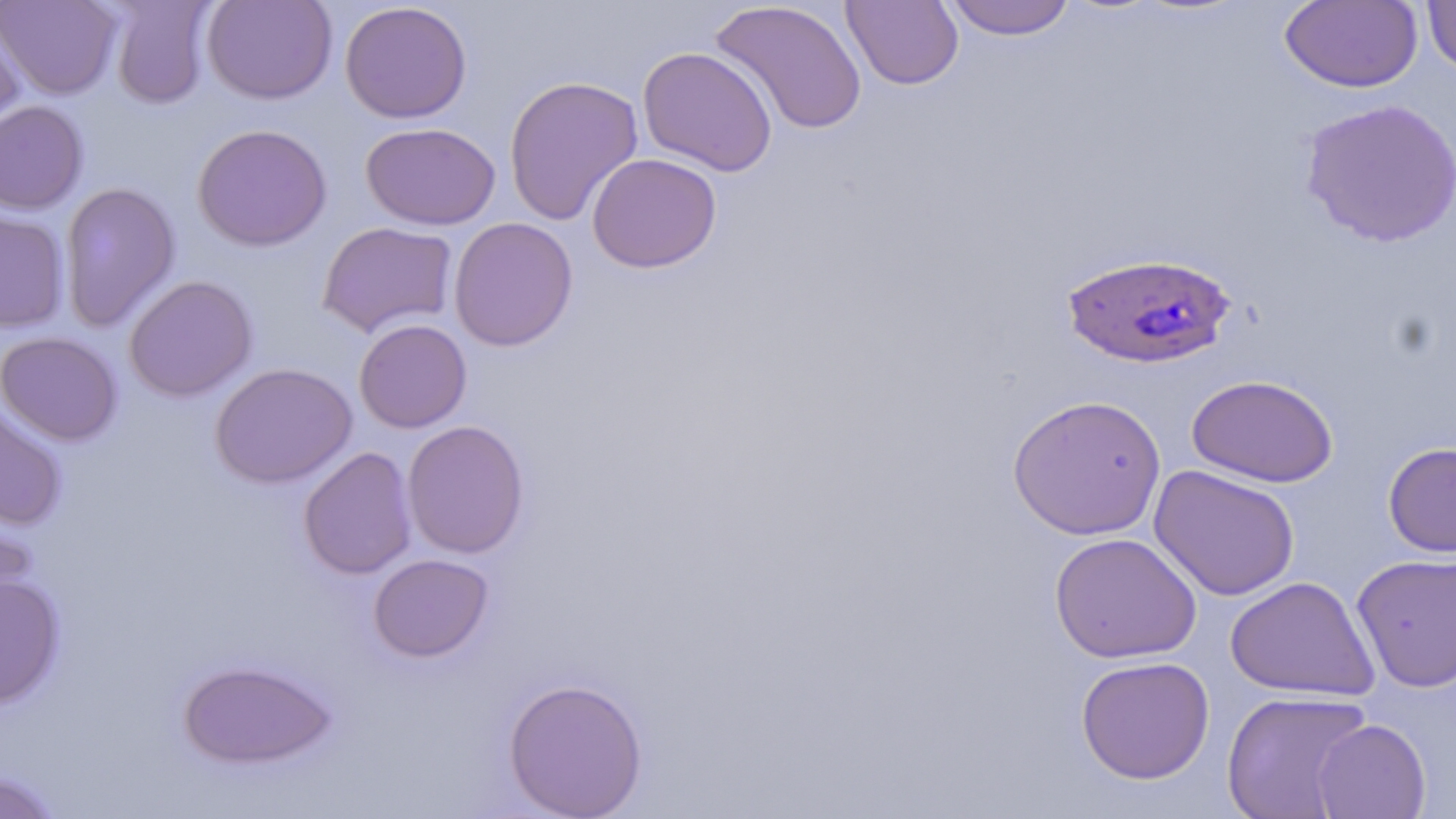
Summary:
  - Coordinate format: approximate bounding boxes as [x1, y1, x2, y2] in pixels
  - Plasmodium falciparum-infected red blood cell locations: [1060, 251, 1237, 369]
  - Uninfected red blood cell locations: [0, 0, 122, 99], [108, 0, 216, 109], [202, 0, 338, 104], [841, 0, 963, 90], [942, 0, 1077, 40], [1421, 0, 1456, 76], [709, 1, 867, 136], [1279, 1, 1423, 93], [340, 2, 472, 124], [0, 13, 27, 136], [638, 46, 778, 176], [504, 74, 644, 227], [1299, 98, 1456, 248], [0, 100, 88, 215], [360, 122, 500, 231], [192, 123, 332, 251], [586, 153, 722, 273], [59, 182, 181, 332], [0, 208, 70, 333], [448, 217, 578, 352], [318, 221, 458, 337], [124, 275, 258, 402], [354, 319, 472, 433], [1, 331, 123, 446], [210, 362, 357, 488], [1186, 374, 1339, 487], [1007, 393, 1166, 540], [0, 401, 68, 530], [402, 419, 530, 558], [1383, 442, 1456, 557], [298, 446, 418, 580], [1149, 464, 1300, 601], [0, 501, 37, 624], [1050, 531, 1202, 663], [368, 553, 494, 662], [1351, 553, 1456, 692], [0, 574, 65, 708], [1225, 576, 1379, 701], [1075, 655, 1215, 784], [177, 659, 337, 770], [503, 677, 648, 819], [1221, 690, 1373, 818], [1311, 718, 1431, 819], [0, 770, 65, 819]
  - Slide-level diagnosis: Plasmodium falciparum
  - Image size: 1456×819 pixels
  - Preparation: thin blood film
  - Modality: optical microscopy
  - Field of view: one of a larger specimen
  - Stain: May-Grünwald-Giemsa
  - Magnification: 1000x